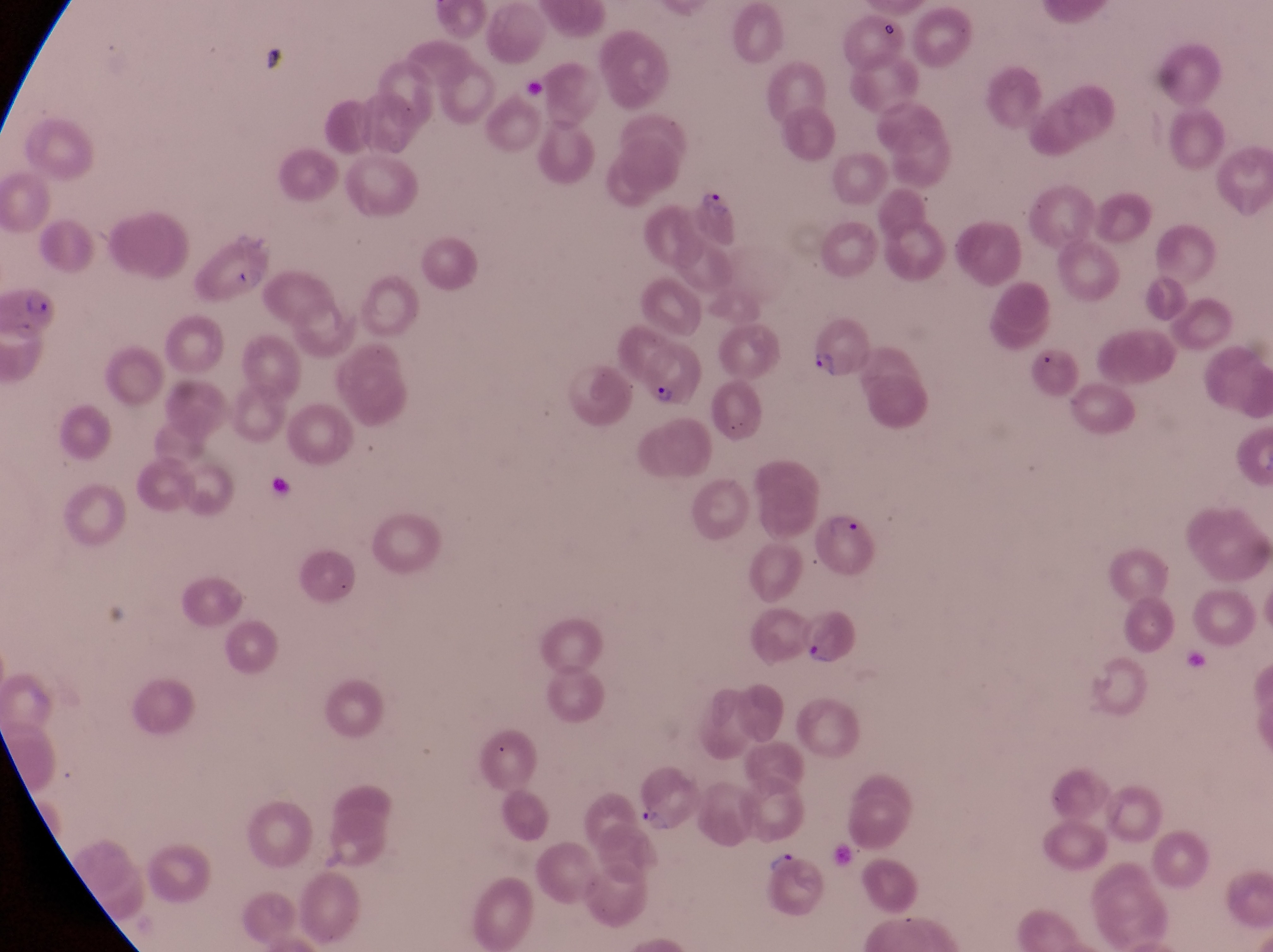

Approximate bounding boxes as (left, top, right, bottom) in pixels. Parasitised red blood cell locations: (691, 174, 746, 246), (182, 230, 272, 302), (0, 283, 57, 343), (808, 317, 873, 385), (637, 342, 702, 407), (813, 507, 883, 582), (794, 602, 859, 672), (632, 766, 702, 836). Artifact (platelet-like body, stain precipitate, or debris) locations: (878, 20, 903, 47), (252, 40, 299, 80). Trophozoite locations: (761, 847, 800, 869). Captured by a smartphone held over the eyepiece of an Olympus CX-23 microscope. Image is 1273×952 pixels. Collected in Uganda. At a magnification of 1000x. Thin blood film. Single field of view.